Assess the morphology of the red blood cells.
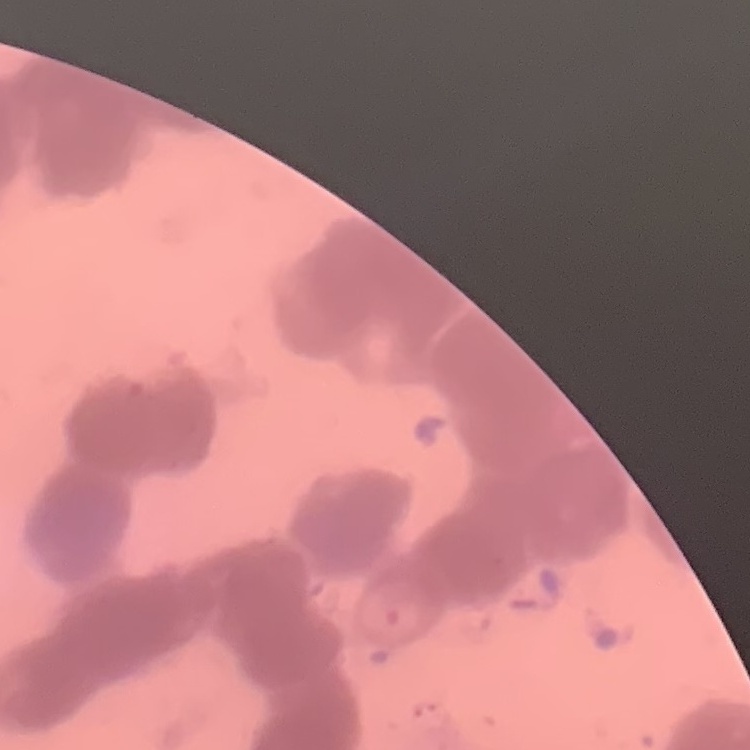

They show rouleaux formation.

Summary:
  - Preparation: thin blood film
  - Image type: one tile cut from a larger photomicrograph
  - Stain: Field's or Giemsa